Name the parasite shown.
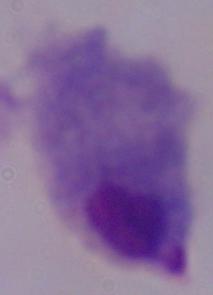

A trichomonad.

magnification: 1000x
modality: micrograph